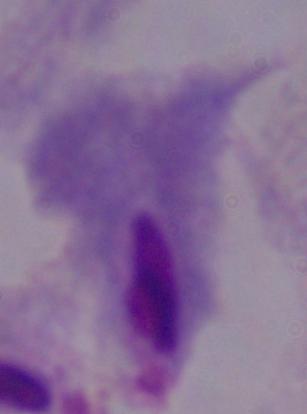 1000x magnification. A trichomonad is seen. Photomicrograph.